State which parasite is depicted.
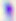
This is Toxoplasma gondii.

modality = micrograph
magnification = 400x